Outline each uninfected red blood cell.
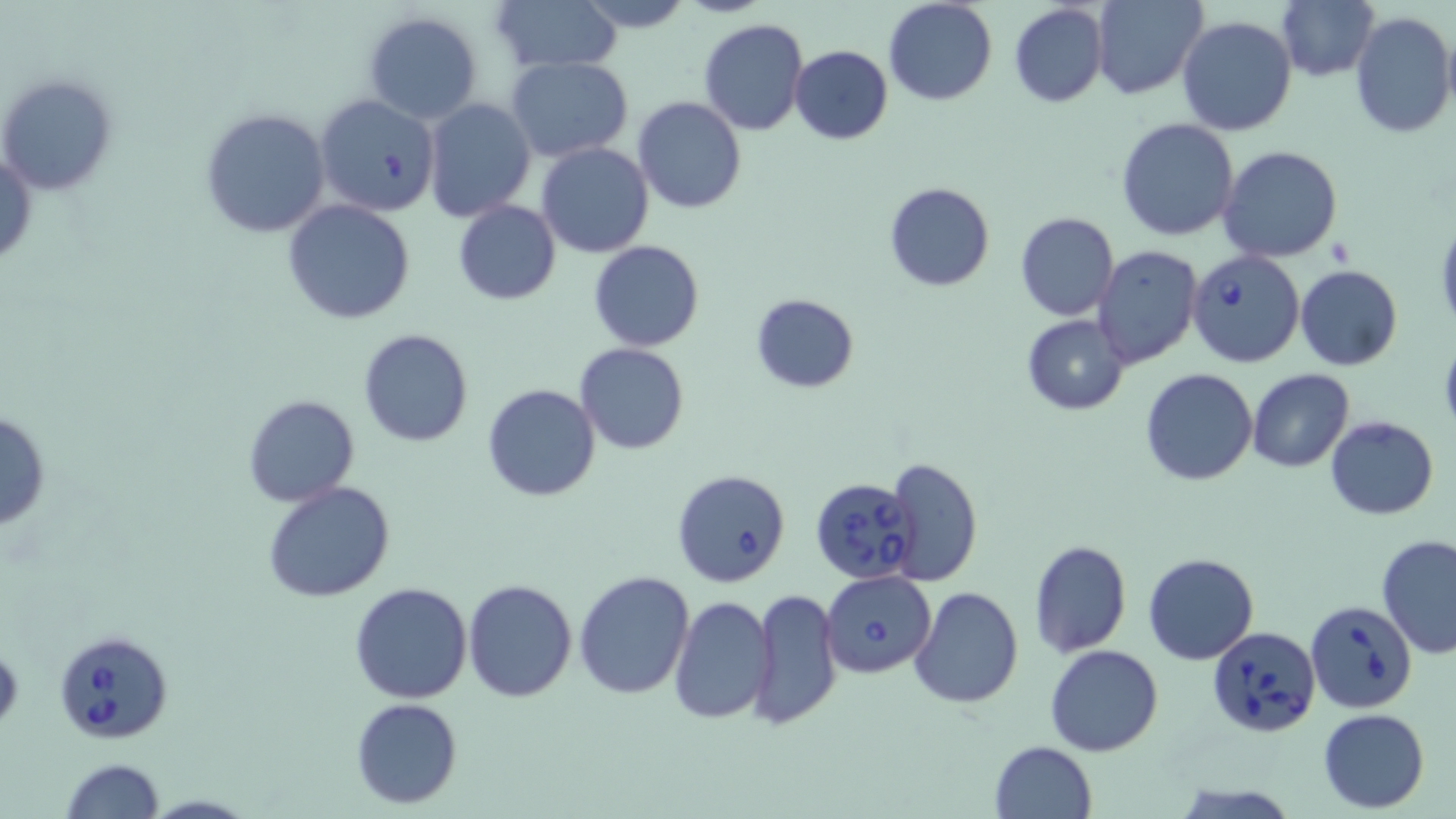

Approximate bounding boxes as (x1,y1)-(x2,y2) corner pairs in pixels.
Uninfected red blood cells: (491,0)-(622,74), (572,0)-(695,33), (882,0)-(998,105), (1276,0)-(1378,83), (1091,1)-(1207,99), (1008,3)-(1109,108), (361,11)-(483,125), (1349,11)-(1456,140), (1176,16)-(1298,137), (698,19)-(808,136), (790,45)-(893,144), (506,55)-(634,163), (0,73)-(118,196), (315,92)-(442,217), (631,94)-(748,214), (421,97)-(536,222), (200,107)-(331,239), (1117,118)-(1239,241), (537,142)-(654,257), (1218,146)-(1343,263), (1,147)-(36,271), (882,181)-(995,291), (282,198)-(415,324), (453,200)-(560,305), (1014,212)-(1120,322), (1433,216)-(1456,333), (589,240)-(704,352), (1094,246)-(1205,369), (1295,265)-(1403,370), (750,293)-(859,394), (1021,314)-(1131,416), (357,327)-(475,448), (575,343)-(689,455), (1139,368)-(1258,487), (1246,369)-(1355,473), (481,382)-(601,502), (243,395)-(360,507), (0,408)-(51,535), (1325,416)-(1438,519), (883,457)-(983,585), (263,481)-(396,604), (1376,534)-(1456,659), (1029,540)-(1131,656), (1142,552)-(1260,666), (573,569)-(694,700), (463,578)-(577,701), (350,581)-(473,702), (908,586)-(1024,710), (747,587)-(843,729), (667,595)-(776,723), (1045,644)-(1164,757), (351,698)-(462,808), (1318,708)-(1430,812), (989,740)-(1096,819), (60,759)-(165,819).

Babesia divergens-infected red blood cell locations: (1185,250)-(1305,368), (671,468)-(792,589), (808,476)-(919,584), (820,570)-(936,678), (1308,600)-(1414,712), (1208,625)-(1320,738), (53,627)-(169,744). Slide-level diagnosis: Babesia divergens. Thin blood smear. One field of a larger specimen. May-Grünwald-Giemsa stain. Light microscopy. Image is 1456×819 pixels. Captured at 1000x magnification.